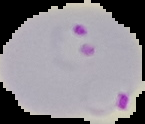
Cell region segmented out of the field of view; the surrounding area is masked to black. Image is 145×124 pixels. Malaria status: parasitized. From a thin blood film.